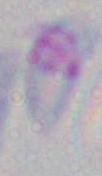
Summary:
  - Modality: photomicrograph
  - Magnification: 1000x
  - Identification: Toxoplasma gondii